Identify the cell.
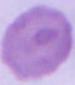
An erythrocyte.

Photomicrograph. Captured at 1000x magnification.